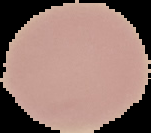

Summary:
  - Image size: 151×133 pixels
  - Malaria status: uninfected
  - Image type: cell region segmented out of the field of view; surrounding area masked to black
  - Preparation: thin blood film